Classify this cell by malaria status.
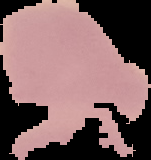

It is uninfected.

From a thin blood smear. The area outside the segmented cell region is set to black. Image is 151×160 pixels.